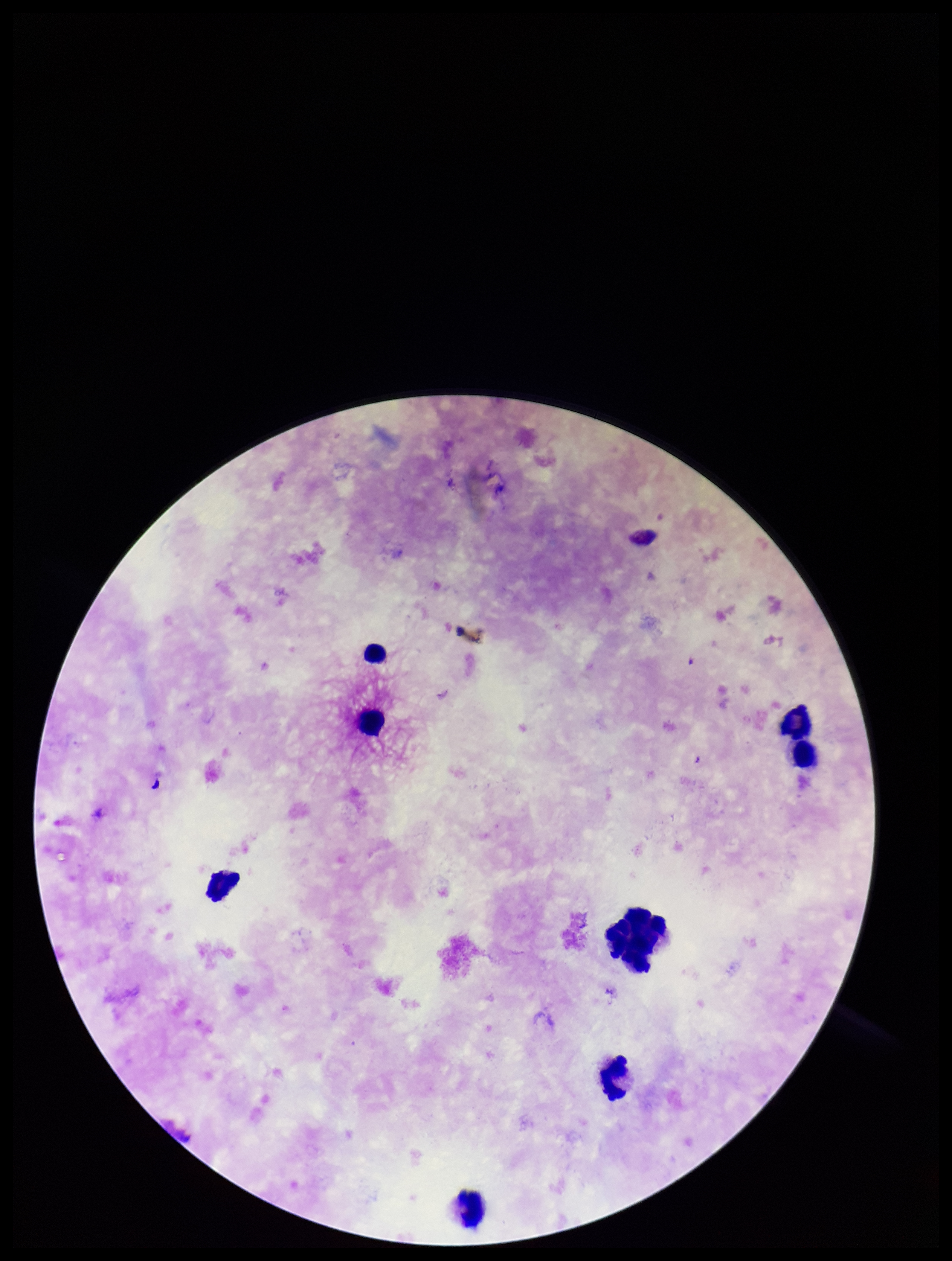

leukocyte count = 8
preparation = thick
stain = Giemsa
patient malaria status = positive
capture = smartphone photograph through the microscope eyepiece
species reported for this patient = Plasmodium falciparum
Plasmodium parasites = none seen
field of view = one from this slide
image size = 952×1261 pixels
parasite count = 0